Outline each blood parasite and name the species.
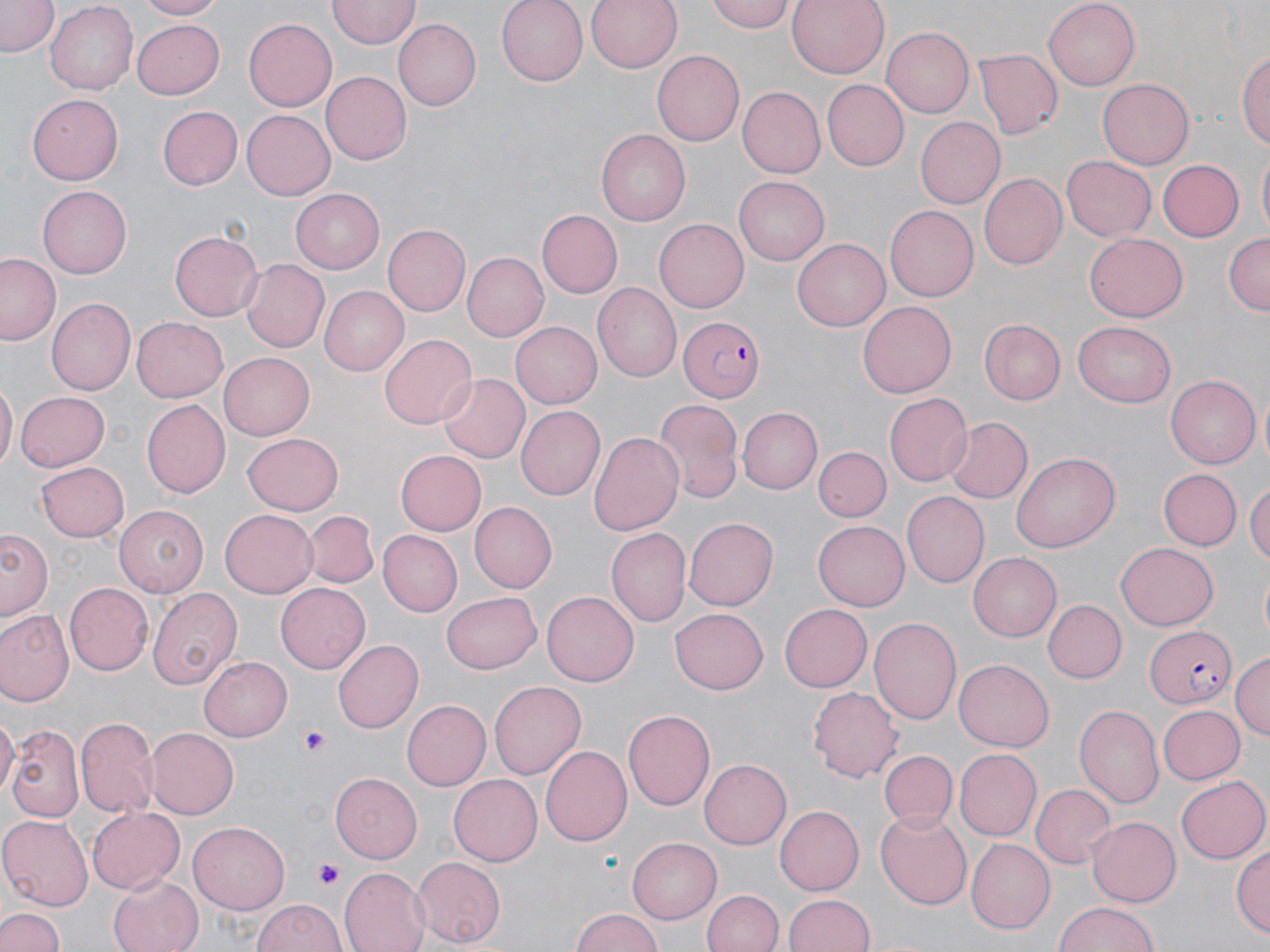

Approximate bounding boxes as (x1, y1, x2, y2) in pixels.
Plasmodium falciparum-infected red blood cells: (677, 317, 766, 401), (1145, 624, 1238, 710).
No Plasmodium ovale, Plasmodium malariae, Plasmodium vivax, Babesia divergens, or Trypanosoma brucei observed.

Uninfected red blood cell locations: (2, 0, 58, 58), (43, 0, 138, 92), (136, 0, 227, 20), (498, 0, 592, 84), (584, 0, 683, 74), (706, 0, 795, 30), (787, 0, 888, 78), (328, 1, 420, 48), (1042, 1, 1139, 91), (132, 18, 225, 99), (243, 18, 337, 111), (393, 19, 480, 110), (881, 26, 974, 118), (1237, 47, 1270, 155), (973, 48, 1064, 140), (652, 50, 747, 145), (322, 71, 412, 165), (1097, 78, 1194, 170), (821, 79, 908, 171), (739, 88, 824, 176), (27, 95, 121, 184), (156, 104, 241, 189), (242, 110, 335, 200), (914, 117, 1005, 210), (595, 132, 688, 225), (1255, 150, 1270, 241), (1058, 154, 1156, 242), (1155, 158, 1245, 242), (977, 172, 1066, 270), (733, 176, 831, 266), (39, 187, 131, 277), (291, 188, 384, 273), (885, 206, 979, 301), (535, 210, 621, 298), (655, 218, 748, 313), (383, 224, 469, 316), (169, 230, 262, 321), (1224, 232, 1270, 315), (1083, 234, 1187, 321), (792, 239, 891, 332), (461, 252, 549, 341), (1, 254, 62, 346), (240, 257, 331, 353), (595, 283, 681, 382), (319, 287, 408, 376), (45, 298, 134, 396), (858, 300, 958, 398), (131, 316, 228, 402), (978, 319, 1066, 405), (1073, 322, 1176, 408), (511, 323, 601, 408), (381, 333, 477, 430), (218, 353, 312, 440), (436, 373, 530, 464), (1165, 374, 1261, 469), (0, 380, 16, 474), (15, 391, 110, 469), (883, 393, 971, 487), (654, 397, 744, 505), (142, 399, 230, 498), (740, 405, 823, 493), (516, 406, 605, 500), (947, 416, 1032, 504), (589, 430, 686, 537), (242, 431, 344, 515), (814, 445, 890, 522), (394, 450, 486, 535), (1012, 450, 1119, 553), (37, 460, 130, 541), (1158, 469, 1240, 551), (1247, 478, 1270, 569), (900, 491, 989, 585), (469, 501, 558, 593), (113, 505, 208, 598), (303, 509, 380, 589), (220, 510, 317, 596), (685, 516, 782, 610), (813, 520, 909, 611), (2, 526, 55, 624), (607, 528, 691, 628), (376, 530, 461, 616), (1116, 539, 1217, 627), (966, 551, 1061, 642), (275, 582, 371, 674), (64, 583, 154, 675), (146, 587, 242, 690), (441, 591, 541, 674), (542, 592, 639, 687), (1042, 599, 1126, 681), (779, 604, 872, 691), (670, 608, 769, 694), (0, 609, 73, 707), (867, 615, 961, 725), (333, 639, 423, 733), (1231, 651, 1270, 741), (199, 655, 293, 741), (954, 660, 1054, 751), (489, 679, 587, 782), (808, 686, 903, 782), (403, 701, 490, 789), (1074, 705, 1163, 810), (1156, 705, 1244, 786), (622, 709, 715, 810), (0, 716, 17, 803), (76, 717, 159, 820), (7, 722, 83, 823), (146, 726, 239, 819), (541, 746, 631, 846), (878, 747, 957, 833), (955, 750, 1041, 839), (699, 759, 791, 849), (329, 773, 422, 863), (450, 774, 541, 866), (1176, 775, 1269, 864), (1030, 782, 1114, 869), (773, 804, 863, 895), (86, 806, 183, 896), (874, 810, 973, 909), (0, 814, 95, 911), (1087, 816, 1181, 905), (187, 820, 290, 914), (627, 837, 721, 923), (964, 839, 1053, 934), (1231, 843, 1270, 938), (410, 857, 506, 947), (340, 868, 430, 952), (106, 874, 204, 952), (701, 889, 784, 952), (785, 894, 876, 952), (252, 898, 346, 952), (1052, 900, 1159, 952), (0, 906, 67, 952), (570, 907, 665, 952). Platelet locations: (301, 726, 330, 758), (317, 862, 347, 890). Slide-level diagnosis: Plasmodium falciparum. May-Grünwald-Giemsa-stained preparation. Thin blood smear. Image is 1270×952 pixels. Light microscopy. Captured at 1000x magnification. Single field of view.